Report the malaria status of this cell.
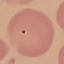

It is uninfected.

stain = Giemsa
capture = smartphone through the microscope eyepiece
image type = cell patch, automatically extracted from a larger field of view and resized to 64 × 64 pixels
preparation = thin blood smear